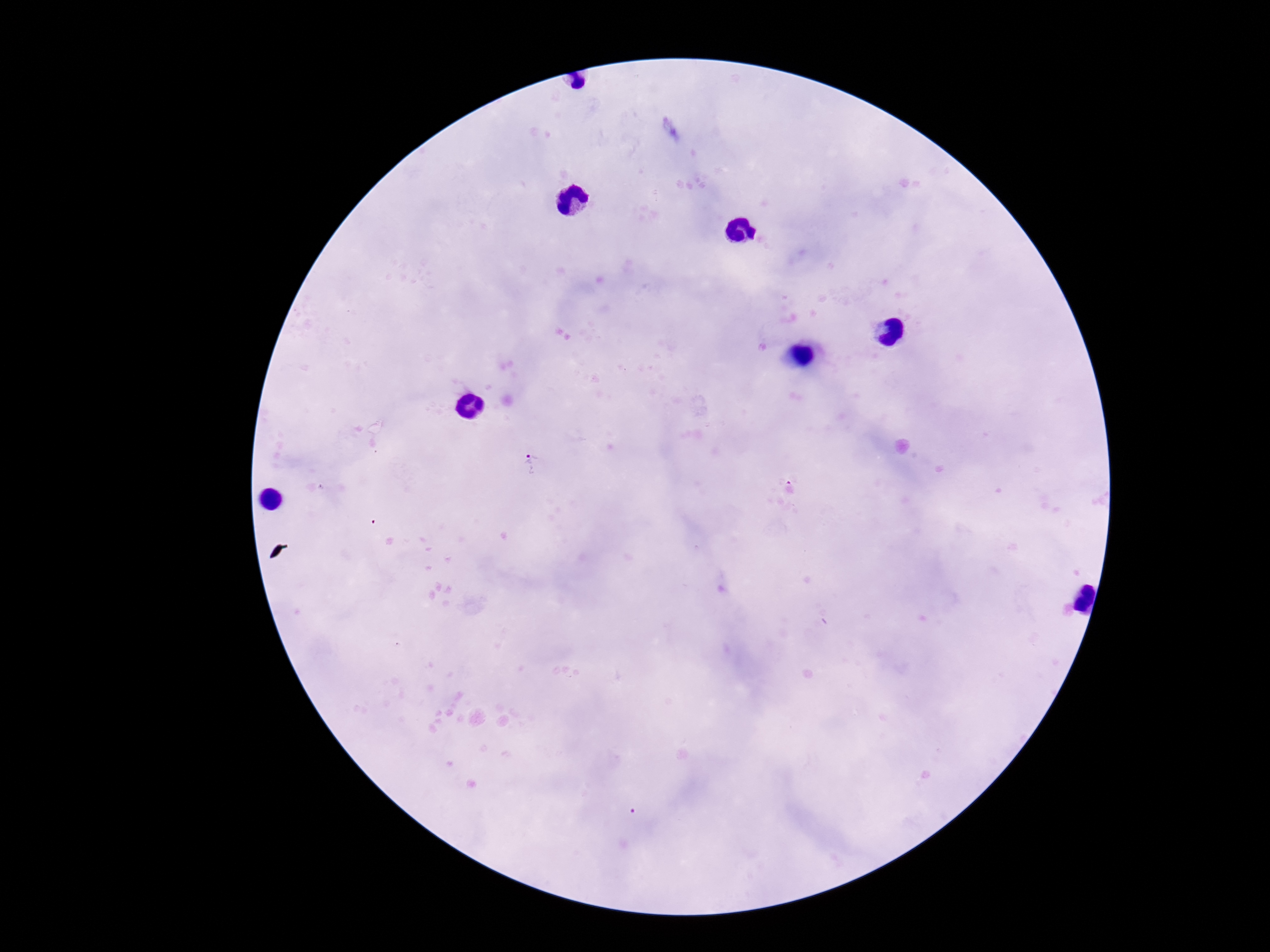

{
  "image_size": "1270×952 pixels",
  "stain": "Giemsa",
  "patient_malaria_status": "positive",
  "field_of_view": "one from this slide",
  "plasmodium_parasite_locations": "approximate object centers, in pixels from the top-left corner: (x=532, y=462), (x=790, y=489), (x=635, y=814)",
  "capture": "smartphone camera through the microscope eyepiece",
  "magnification": "100x",
  "preparation": "thick blood film"
}